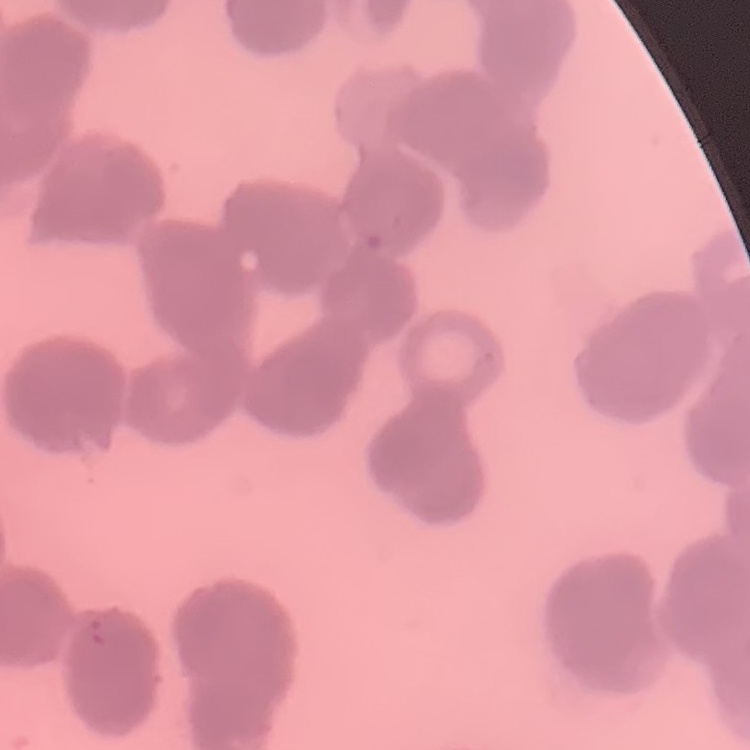

red blood cell morphology = rouleaux formation
stain = Field's or Giemsa
image type = square crop of a larger photomicrograph
preparation = thin blood smear